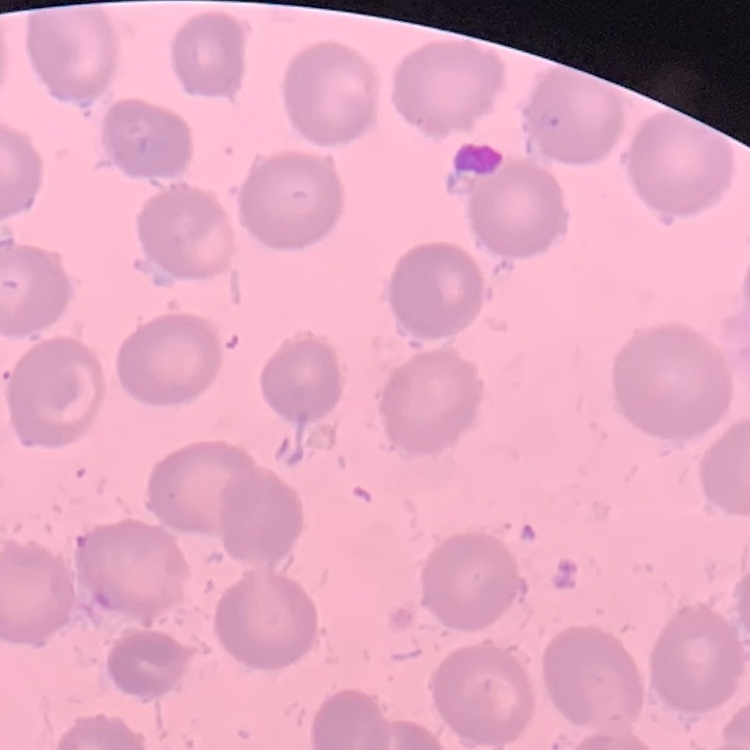
Summary:
  - Erythrocyte morphology: no rouleaux formation
  - Preparation: thin blood film
  - Stain: Field's or Giemsa
  - Image type: one tile cut from a larger photomicrograph